State the blood parasite species.
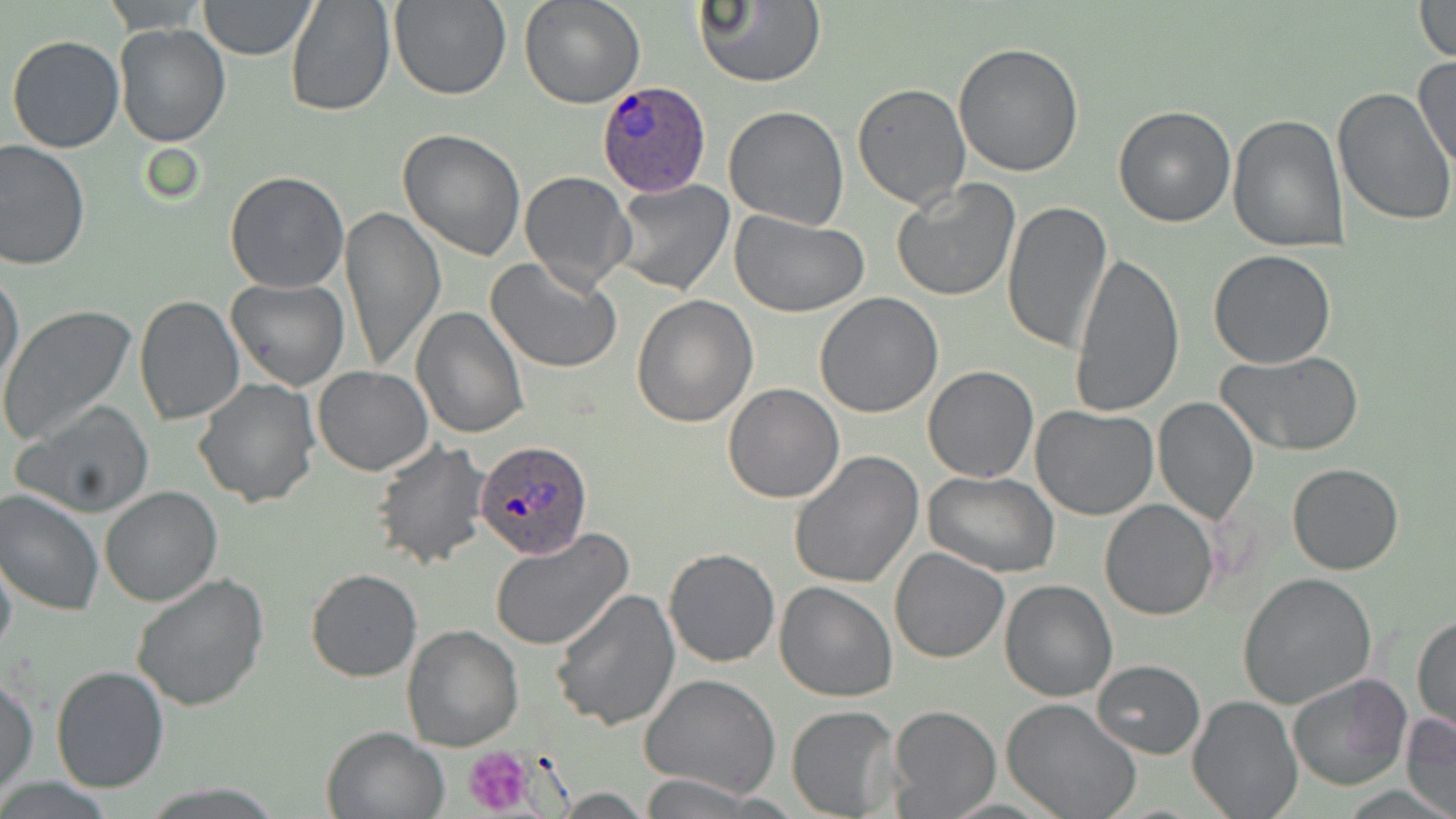
Plasmodium ovale.

Summary:
  - Coordinate format: approximate bounding boxes as (x1,y1)-(x2,y2) corner pairs in pixels
  - Plasmodium ovale-infected red blood cell locations: (594,80)-(713,197), (475,439)-(591,561)
  - Platelet locations: (463,745)-(539,816)
  - Uninfected red blood cell locations: (101,0)-(209,33), (285,0)-(396,118), (388,0)-(510,101), (519,0)-(645,109), (691,0)-(825,90), (198,1)-(317,59), (1411,1)-(1456,63), (113,23)-(231,148), (6,34)-(126,154), (953,43)-(1085,178), (1414,54)-(1456,175), (853,83)-(971,212), (1332,88)-(1456,229), (1112,104)-(1236,228), (723,105)-(851,230), (1228,113)-(1348,251), (397,129)-(527,262), (0,139)-(92,270), (519,171)-(635,292), (224,172)-(349,294), (892,178)-(1021,302), (609,180)-(736,297), (1001,199)-(1114,354), (339,206)-(445,372), (729,209)-(871,316), (1207,250)-(1337,369), (1069,251)-(1186,420), (488,255)-(623,373), (0,268)-(25,392), (225,278)-(348,391), (814,293)-(944,418), (631,295)-(759,428), (133,297)-(244,425), (409,305)-(529,439), (0,306)-(136,447), (1217,350)-(1365,457), (921,365)-(1038,483), (312,366)-(432,476), (192,376)-(320,507), (722,382)-(845,503), (1153,396)-(1258,523), (12,401)-(156,519), (1030,405)-(1159,520), (371,440)-(491,570), (788,451)-(924,589), (1288,462)-(1405,575), (923,472)-(1062,578), (101,485)-(222,606), (0,489)-(104,617), (1099,499)-(1220,621), (490,528)-(634,652), (663,546)-(781,667), (889,547)-(1010,663), (0,549)-(17,662), (304,569)-(421,681), (131,572)-(269,711), (1237,572)-(1377,710), (1000,579)-(1118,702), (773,582)-(897,702), (549,588)-(679,729), (1413,614)-(1455,737), (402,626)-(524,750), (1092,659)-(1205,758), (51,665)-(169,794), (1286,671)-(1413,793), (640,674)-(781,799), (1,675)-(39,794), (1188,695)-(1301,818), (1001,697)-(1144,819), (787,705)-(900,817), (886,705)-(1001,817), (1402,710)-(1456,819), (321,726)-(449,819), (637,774)-(768,817)
  - Field of view: one of a larger specimen
  - Preparation: thin blood film
  - Magnification: 1000x
  - Modality: light microscopy
  - Image size: 1456×819 pixels
  - Stain: May-Grünwald-Giemsa